Comment on the morphology of the erythrocytes.
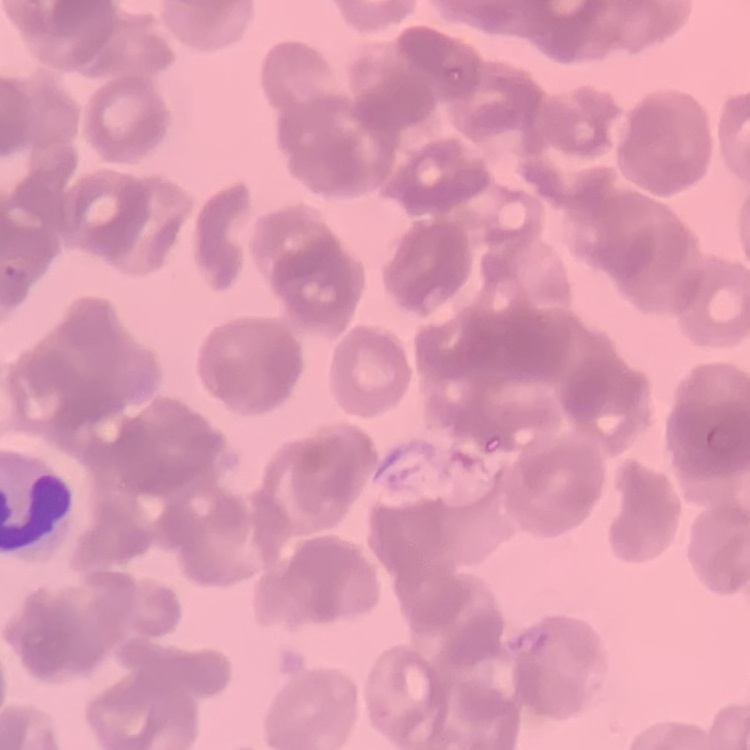

Rouleaux formation.

image_type: square crop of a larger photomicrograph
preparation: thin blood smear
stain: Field's or Giemsa